Identify the parasite.
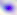

Toxoplasma gondii.

Captured at 400x magnification. Photomicrograph.